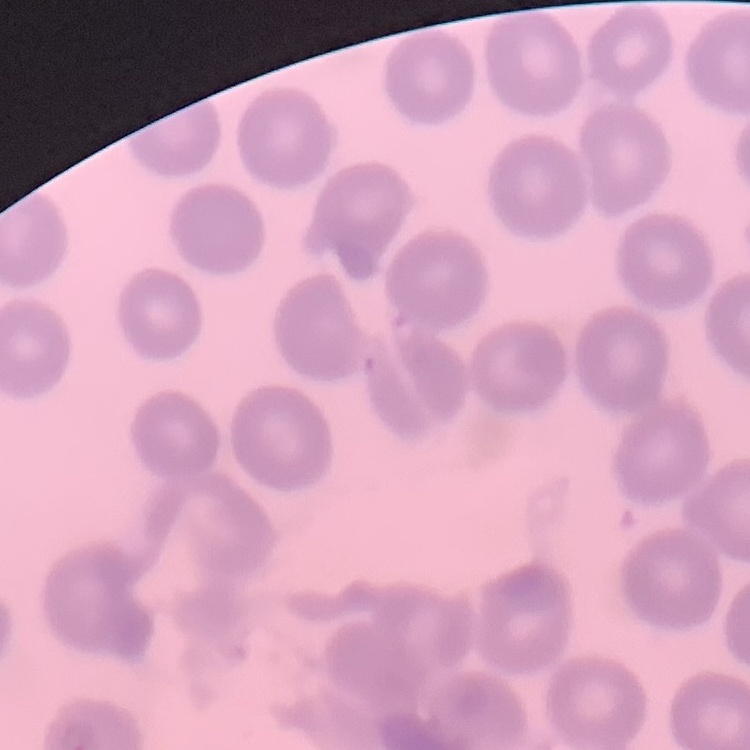

The red blood cells exhibit no rouleaux formation. One tile cut from a larger photomicrograph. Thin blood film. Field's or Giemsa stain.